Describe the morphology of the red blood cells.
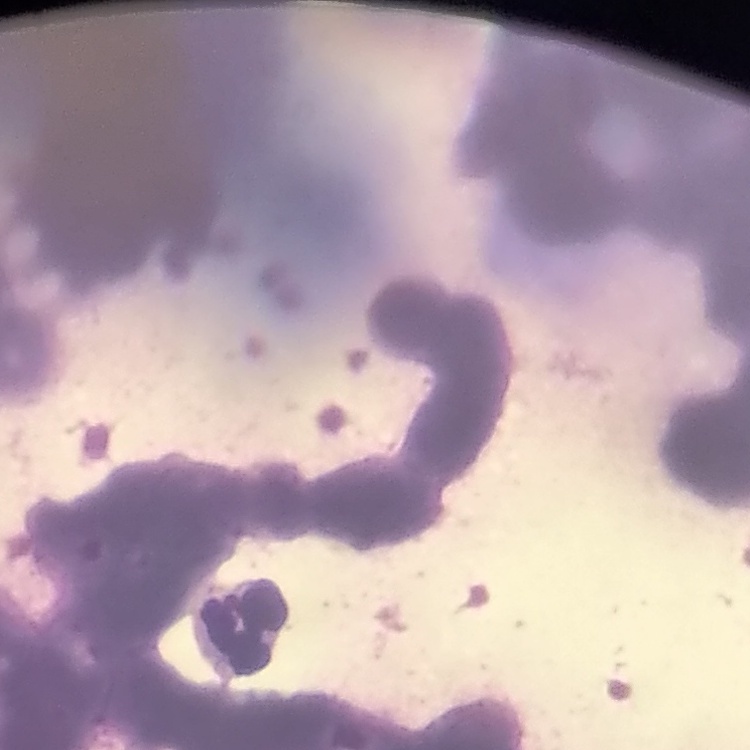
Rouleaux formation.

{
  "stain": "Field's or Giemsa",
  "image_type": "square crop of a larger photomicrograph",
  "preparation": "thin blood film"
}